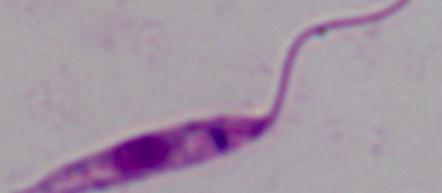
Captured at 1000x magnification. A Leishmania parasite is shown. Photomicrograph.